Assess for malaria.
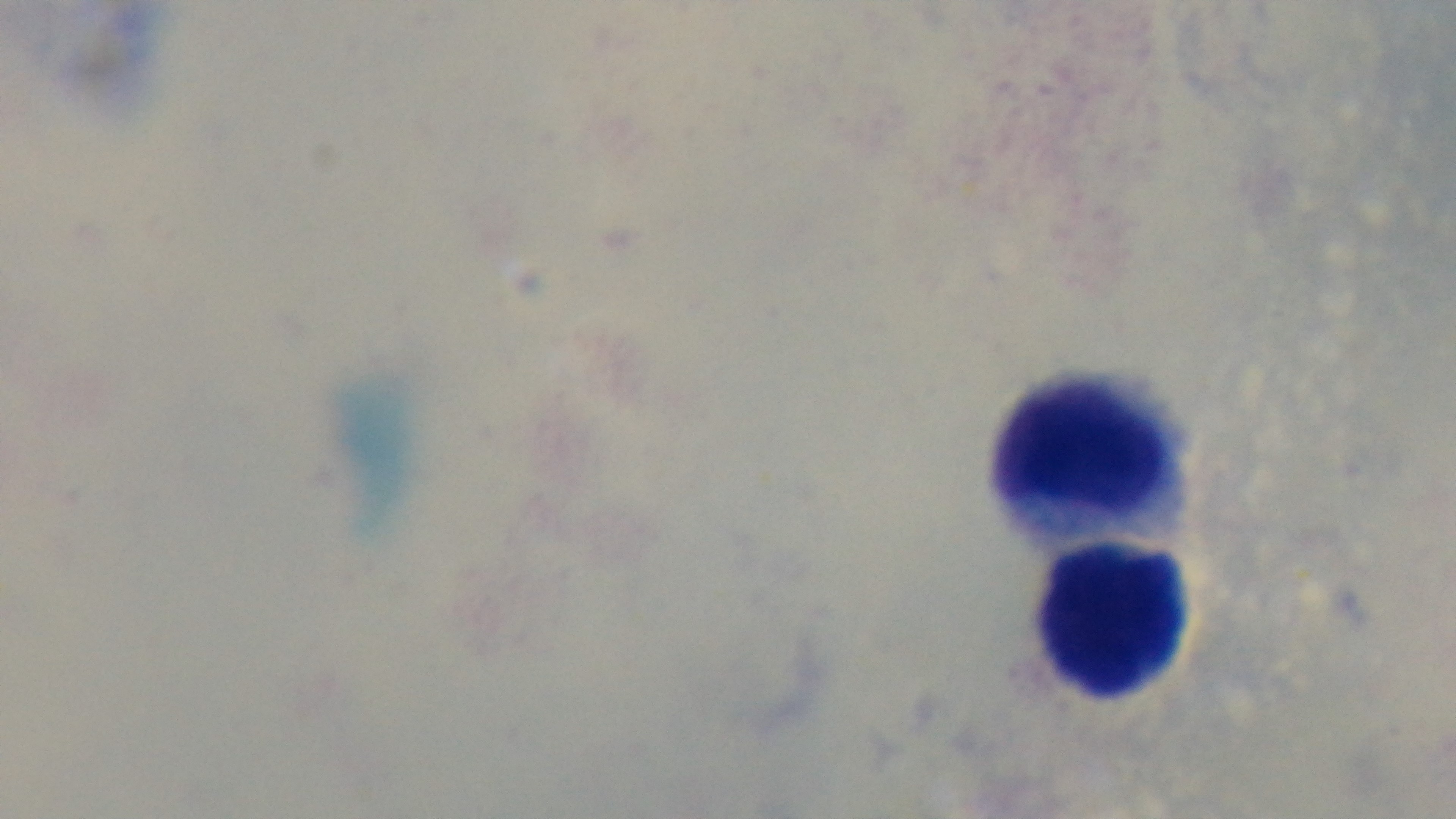
Negative.

Summary:
  - Field of view: one from the slide
  - Modality: light microscopy
  - Capture: mounted 4K digital camera
  - Objective: 100x oil immersion
  - Preparation: thick smear
  - Stain: Giemsa